Identify the parasite.
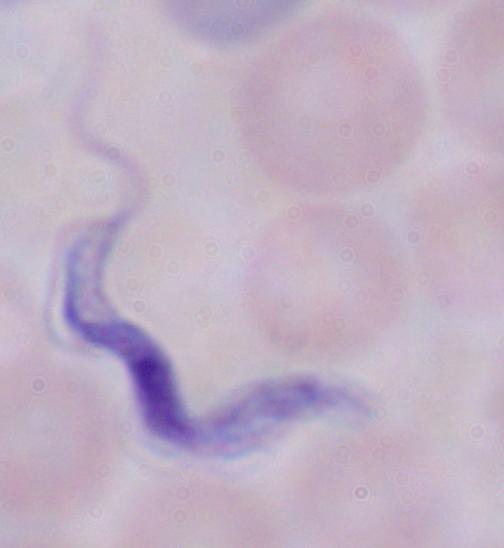

This is a trypanosome.

Summary:
  - Modality: photomicrograph
  - Magnification: 1000x